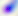

magnification = 400x
identification = Toxoplasma gondii
modality = micrograph